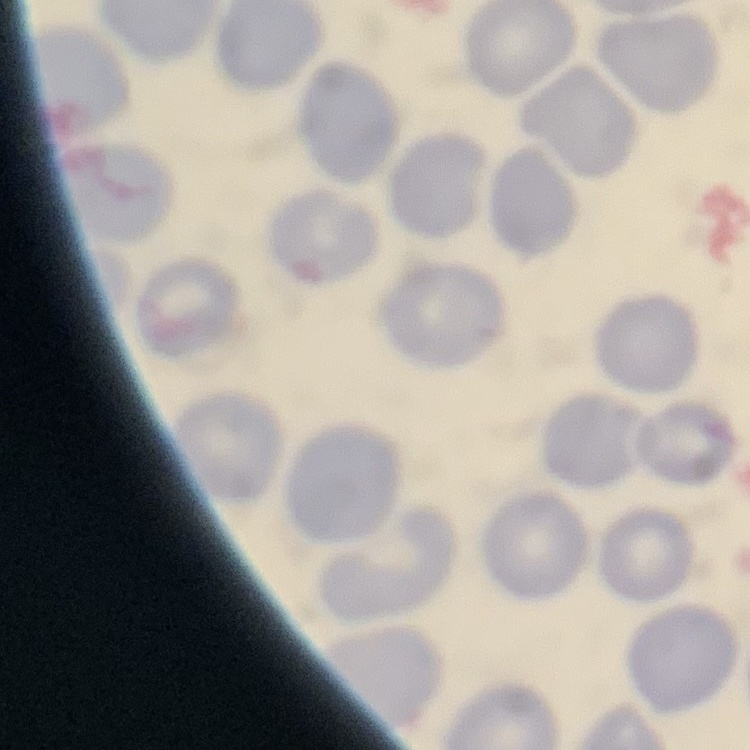
red blood cell morphology = no rouleaux formation
image type = square crop of a larger photomicrograph
stain = Field's or Giemsa
preparation = thin blood film